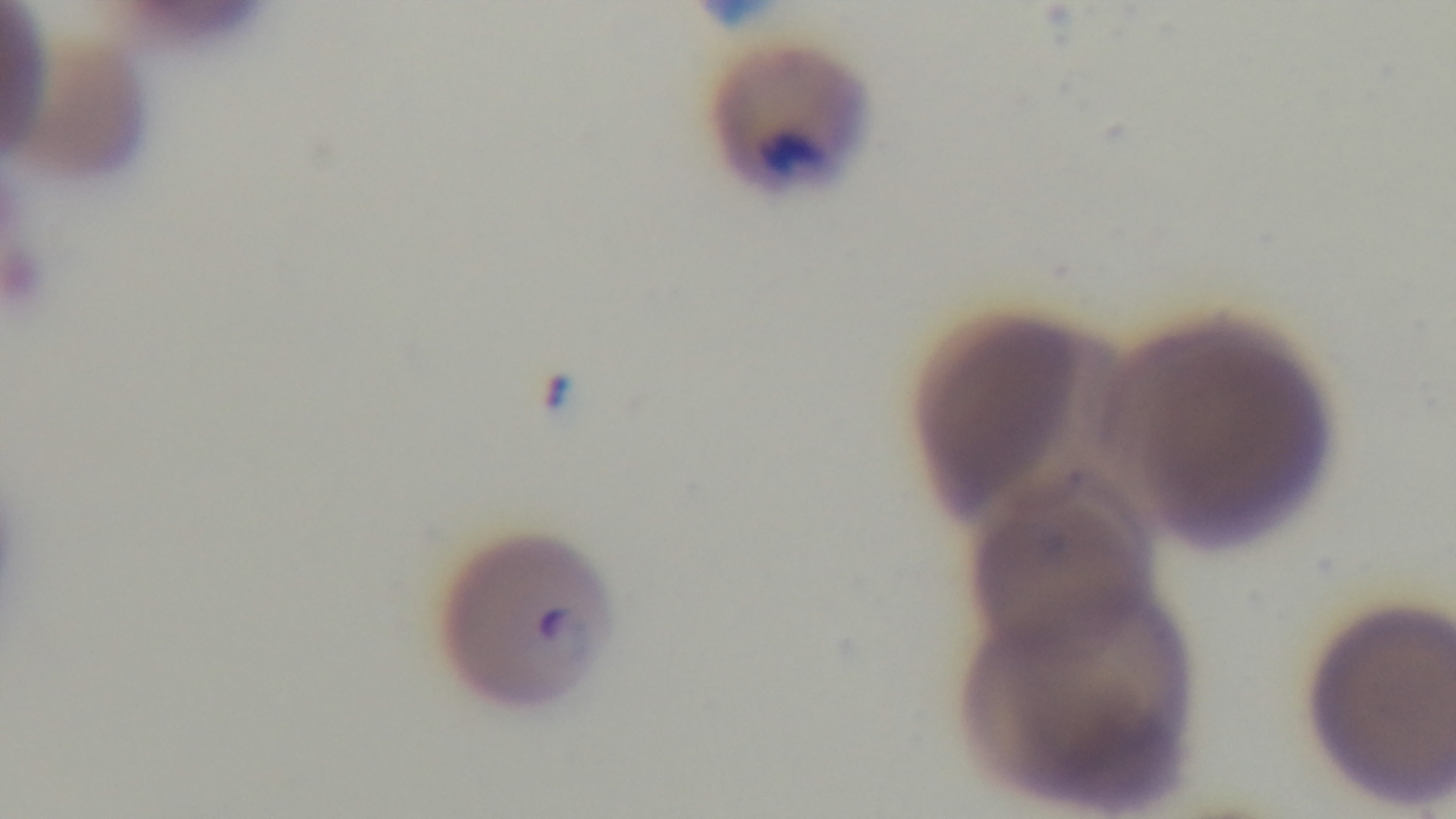 Preparation: thin blood film. Captured with a mounted 4K digital camera. Light microscopy. Malaria status: infected. 100x oil-immersion objective. Giemsa stain. Single field of view.